Point out each malaria parasite.
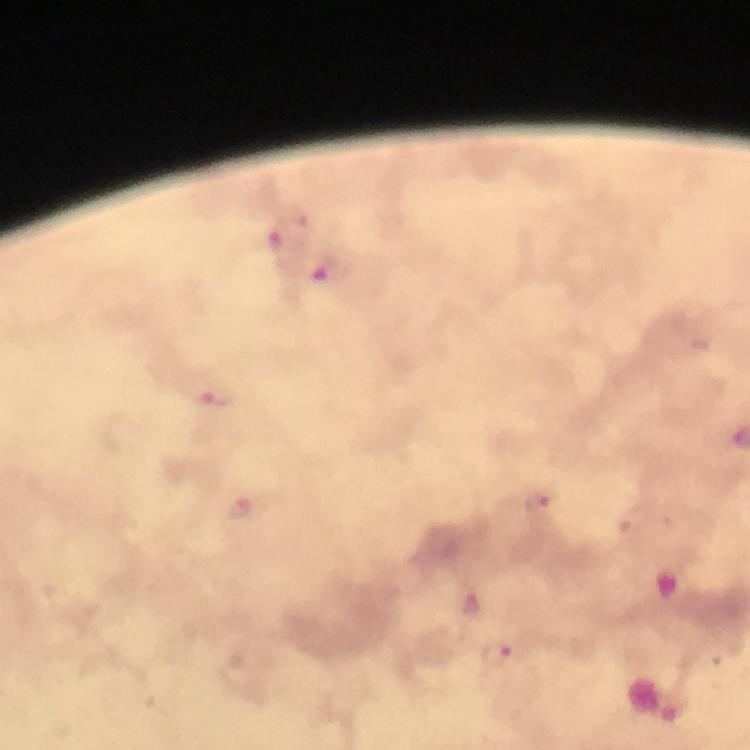

Approximate centers as [x, y] in pixels.
Malaria parasites: [274, 238], [330, 271], [220, 396], [538, 500], [238, 508], [635, 519], [474, 602], [497, 655].

Photographed with a smartphone mounted on the microscope. Thick blood film. Image is 750×750 pixels. From a malaria diagnostic workup. Giemsa stain. At 100x magnification. A crop from one field of view. Immersion oil applied.